Describe the morphology of the erythrocytes.
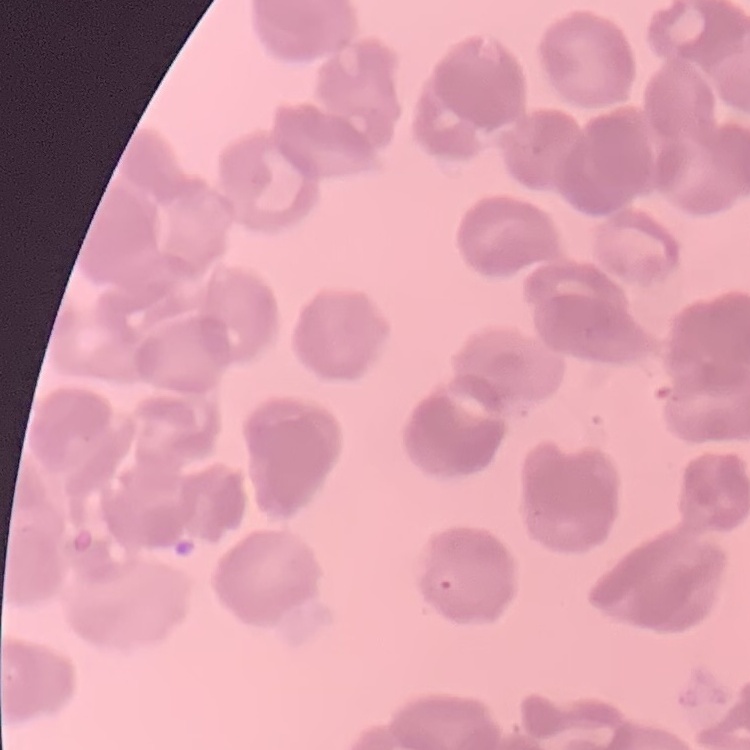
They show rouleaux formation.

Summary:
  - Stain: Field's or Giemsa
  - Preparation: thin blood smear
  - Image type: one tile cut from a larger photomicrograph